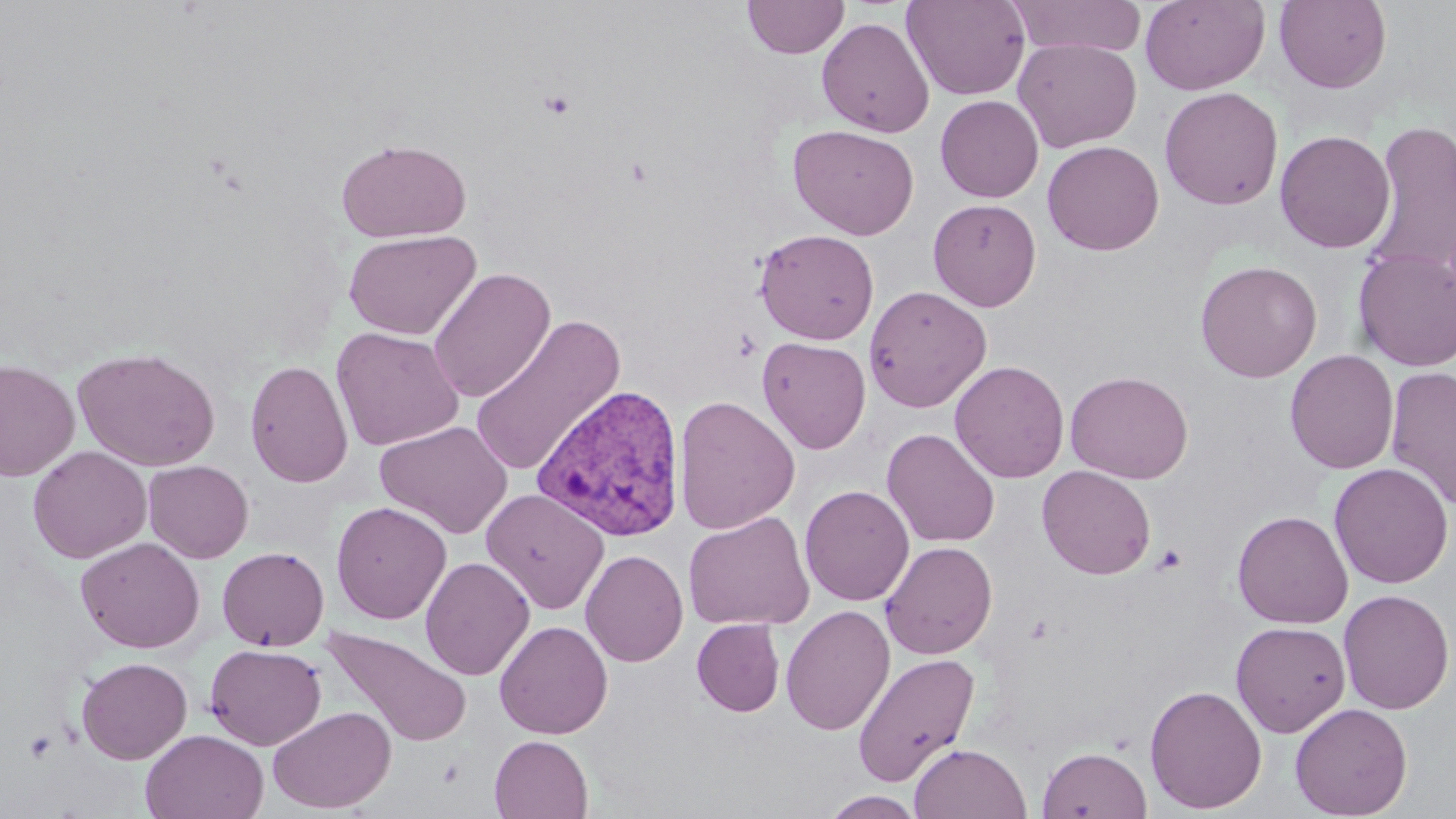 Approximate bounding boxes as (x1, y1, x2, y2) in pixels. Plasmodium vivax-infected red blood cell locations: (532, 383, 688, 543). Uninfected red blood cell locations: (742, 0, 849, 58), (902, 0, 1031, 101), (1005, 0, 1147, 57), (1140, 0, 1269, 95), (1274, 0, 1392, 93), (816, 16, 935, 137), (1013, 38, 1141, 152), (1159, 87, 1284, 210), (935, 95, 1044, 202), (1363, 120, 1456, 279), (787, 124, 920, 240), (1274, 130, 1396, 253), (335, 137, 471, 243), (1042, 140, 1164, 255), (928, 198, 1042, 311), (754, 228, 879, 345), (343, 230, 482, 340), (1353, 249, 1456, 372), (1194, 260, 1322, 383), (427, 267, 556, 403), (863, 285, 992, 412), (469, 315, 625, 477), (330, 327, 465, 451), (757, 336, 871, 454), (72, 347, 220, 471), (1285, 350, 1399, 474), (1, 358, 80, 482), (245, 360, 353, 488), (949, 360, 1069, 483), (1385, 366, 1456, 511), (1065, 370, 1193, 483), (673, 395, 800, 535), (374, 420, 513, 539), (882, 427, 1000, 547), (27, 445, 151, 563), (143, 460, 254, 563), (1329, 462, 1453, 589), (1037, 465, 1157, 579), (799, 484, 915, 606), (481, 489, 609, 614), (331, 501, 452, 625), (1232, 509, 1354, 629), (683, 511, 815, 631), (75, 536, 206, 654), (880, 541, 998, 659), (216, 546, 329, 651), (581, 549, 688, 667), (420, 556, 535, 681), (1338, 589, 1454, 714), (780, 604, 895, 736), (692, 619, 785, 717), (494, 620, 613, 739), (1230, 621, 1351, 737), (321, 625, 472, 748), (205, 643, 326, 750), (851, 652, 979, 787), (76, 656, 192, 764), (1144, 683, 1267, 814), (1289, 702, 1413, 818), (267, 705, 396, 814), (141, 729, 269, 819), (489, 735, 594, 819), (909, 743, 1032, 819), (1037, 746, 1152, 819), (821, 791, 925, 818). Platelet locations: (539, 90, 577, 118), (1151, 544, 1186, 575), (23, 730, 58, 764). Slide-level diagnosis: Plasmodium vivax. May-Grünwald-Giemsa-stained preparation. Captured at 1000x magnification. One field of a larger specimen. Optical microscopy. Image is 1456×819 pixels. Thin blood smear.